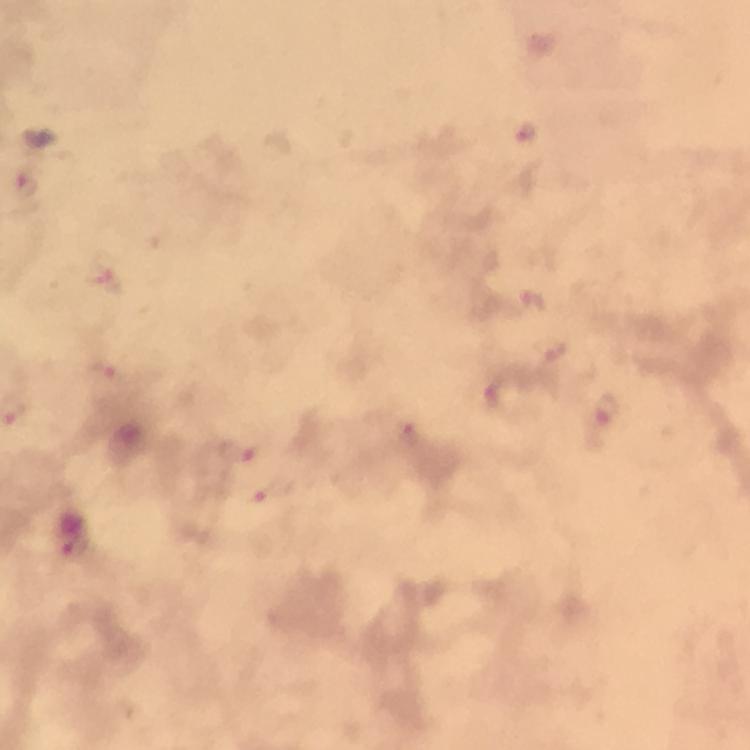
Approximate object centers, in pixels from the top-left corner.
Summary:
  - Plasmodium parasite locations: (x=526, y=132), (x=26, y=185), (x=109, y=283), (x=532, y=301), (x=554, y=356), (x=106, y=370), (x=496, y=393), (x=609, y=411), (x=409, y=436), (x=237, y=451), (x=274, y=493)
  - Preparation: thick smear
  - Cropped from: a single field of view
  - Stain: Giemsa
  - Context: from a diagnostic examination for malaria
  - Magnification: 100x
  - Image size: 750×750 pixels
  - Capture: smartphone photograph through a microscope
  - Immersion oil: applied